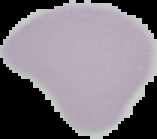
Summary:
  - Image type: segmented cell region with the area outside set to black
  - Malaria status: uninfected
  - Preparation: thin blood smear
  - Image size: 157×139 pixels